Identify the parasite.
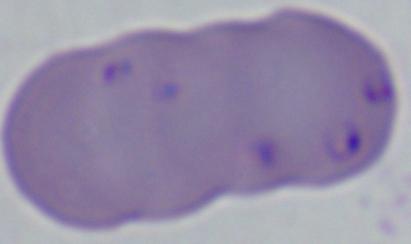

This is Babesia.

magnification = 1000x
modality = micrograph